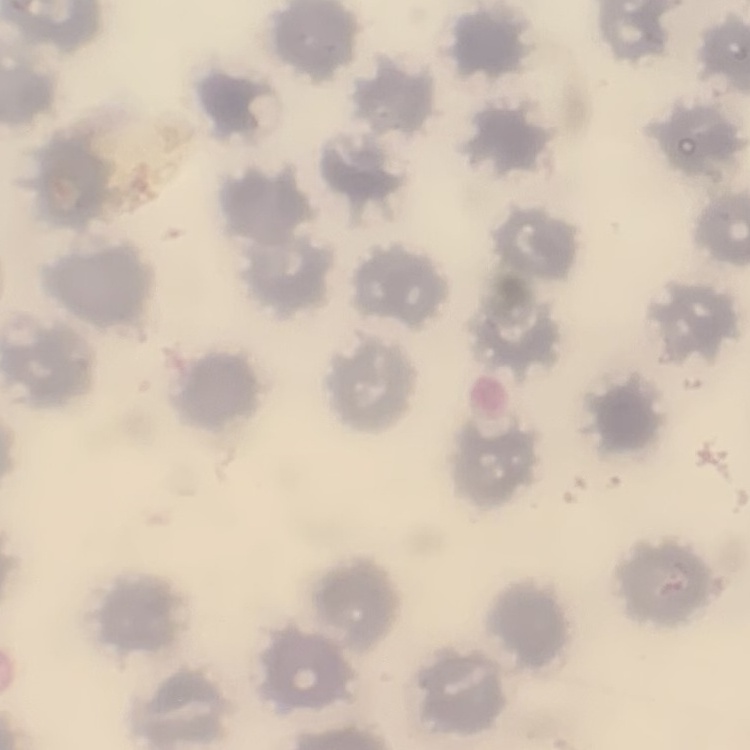
red_blood_cell_morphology: no rouleaux formation
preparation: thin peripheral smear
image_type: square crop of a larger photomicrograph
stain: Field's or Giemsa